State which cell type is depicted.
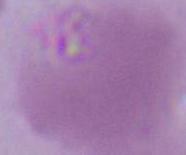

An erythrocyte.

Summary:
  - Magnification: 1000x
  - Modality: photomicrograph